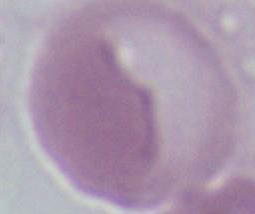

1000x magnification. Micrograph. A red blood cell is shown.